Draw a bounding box around every leukocyte (white blood cell).
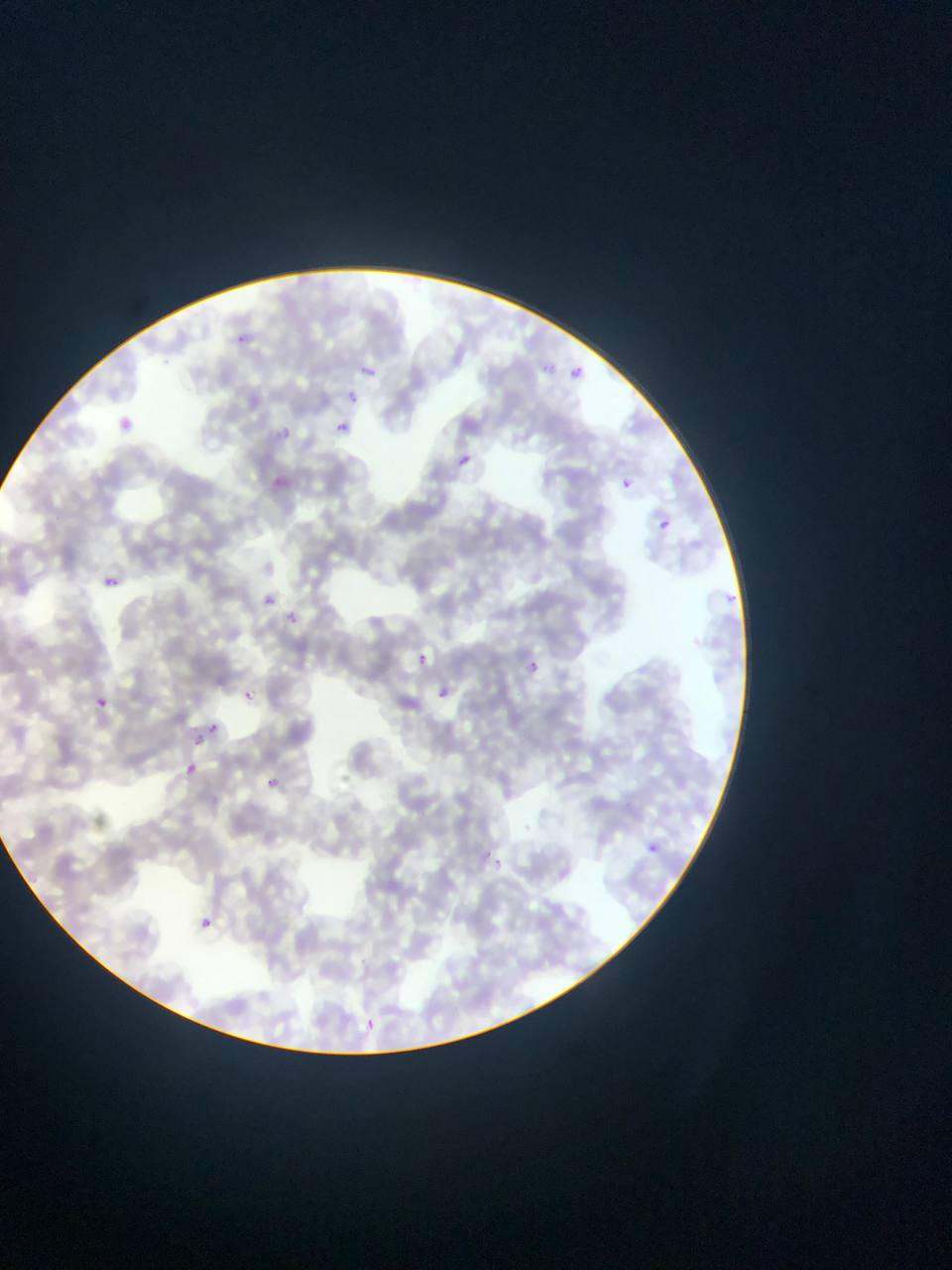

No leukocytes observed.

Approximate bounding boxes as [left, top, right, bottom] in pixels.
Summary:
  - Malaria parasite locations: [534, 358, 559, 381], [356, 359, 383, 383], [570, 360, 584, 380], [344, 387, 364, 408], [110, 412, 142, 440], [332, 419, 351, 437], [274, 426, 292, 442], [456, 453, 471, 467], [614, 475, 635, 495], [651, 513, 675, 536], [102, 575, 118, 589], [721, 584, 746, 605], [256, 589, 280, 610], [282, 608, 301, 628], [409, 647, 435, 671], [525, 660, 540, 674], [434, 686, 449, 703], [242, 690, 254, 701], [90, 694, 109, 711], [207, 723, 219, 734], [183, 762, 199, 777], [265, 779, 275, 787], [646, 843, 659, 855], [494, 854, 508, 865], [192, 912, 219, 937], [355, 1011, 384, 1038]
  - Field of view: single
  - Capture: mobile-phone photograph through a microscope
  - Country: Ghana
  - Image size: 952×1270 pixels
  - Preparation: thin blood smear